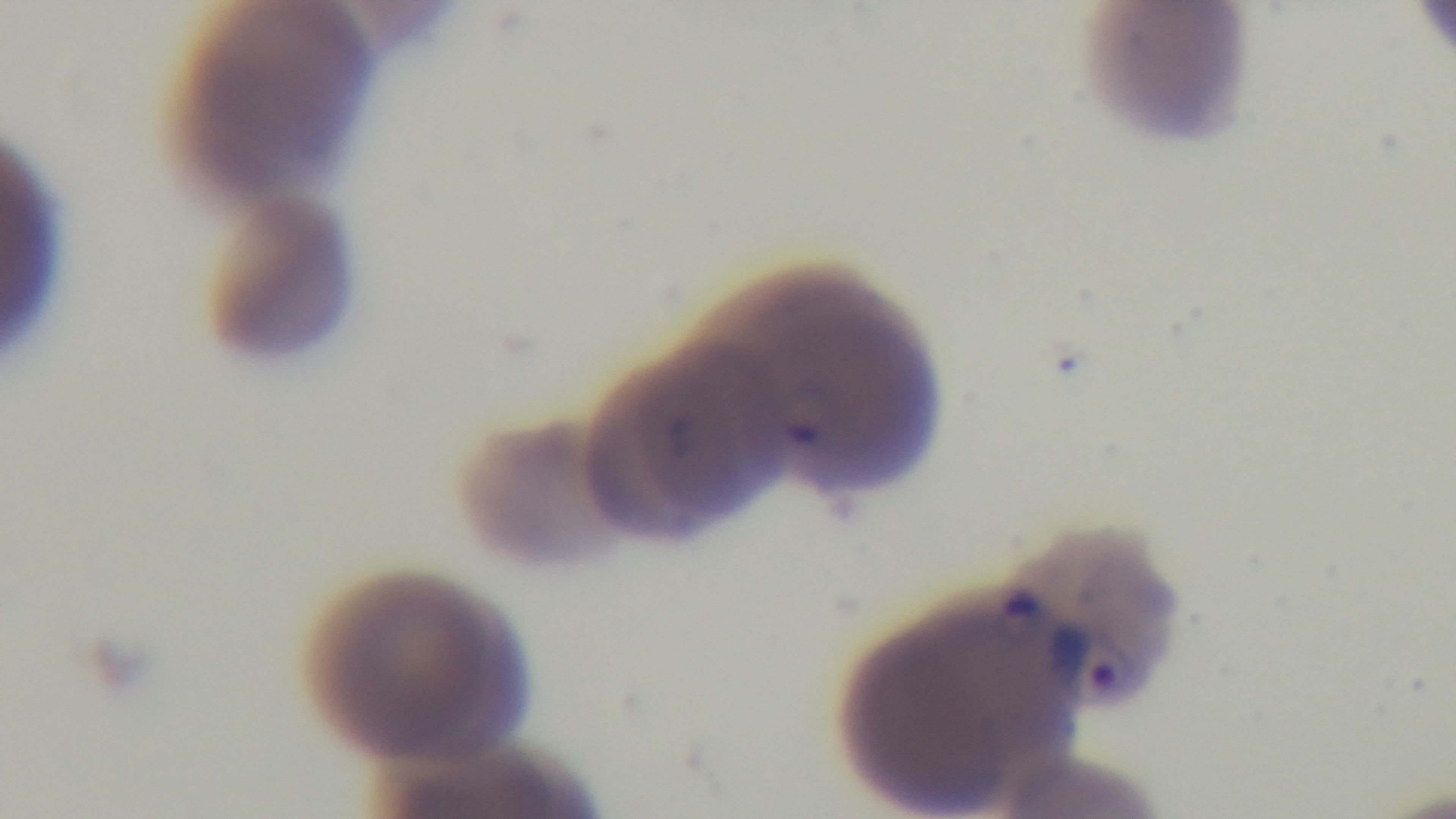

{
  "field_of_view": "one from the slide",
  "capture": "mounted 4K digital camera",
  "stain": "Giemsa",
  "objective": "100x oil immersion",
  "malaria_status": "infected",
  "modality": "light microscopy",
  "preparation": "thin blood film"
}